Comment on the morphology of the erythrocytes.
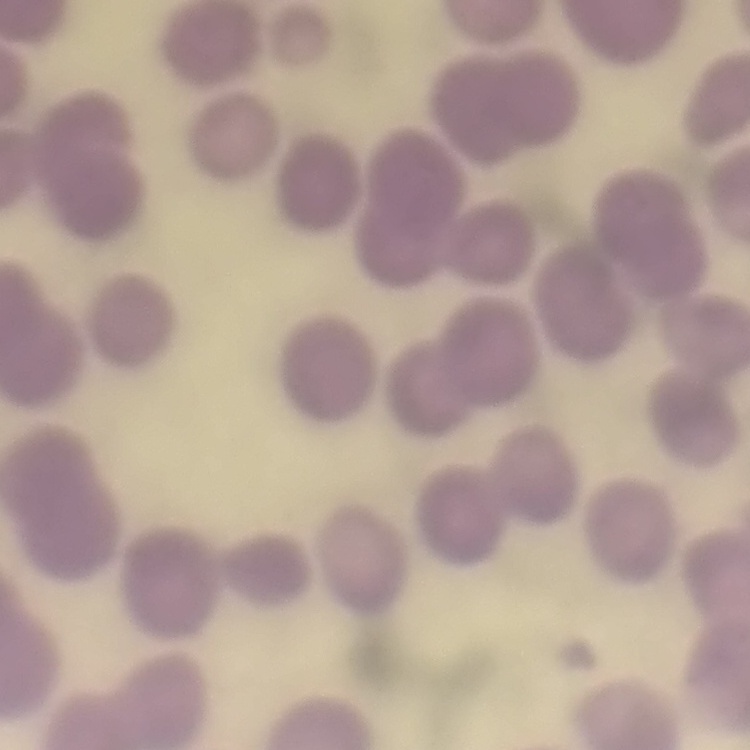
No rouleaux formation.

image type = square crop of a larger photomicrograph
preparation = thin blood smear
stain = Field's or Giemsa